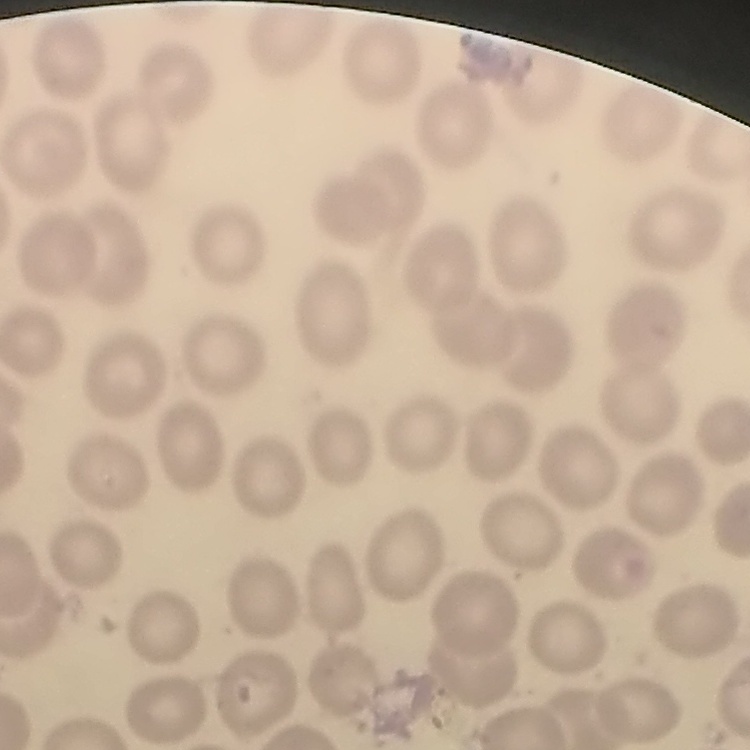

Summary:
  - Red blood cell morphology: no rouleaux formation
  - Image type: square crop of a larger photomicrograph
  - Preparation: thin peripheral smear
  - Stain: Field's or Giemsa